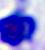

Summary:
  - Identification: white blood cell
  - Magnification: 400x
  - Modality: photomicrograph